Report the malaria status of this cell.
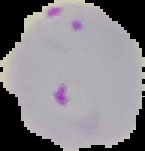
It is parasitized.

Segmented cell region on a black background. From a thin blood film. Image is 145×151 pixels.